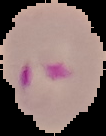
The area outside the segmented cell region is set to black. Image is 106×136 pixels. Malaria status: parasitized. From a thin blood film.